Identify the blood parasite species.
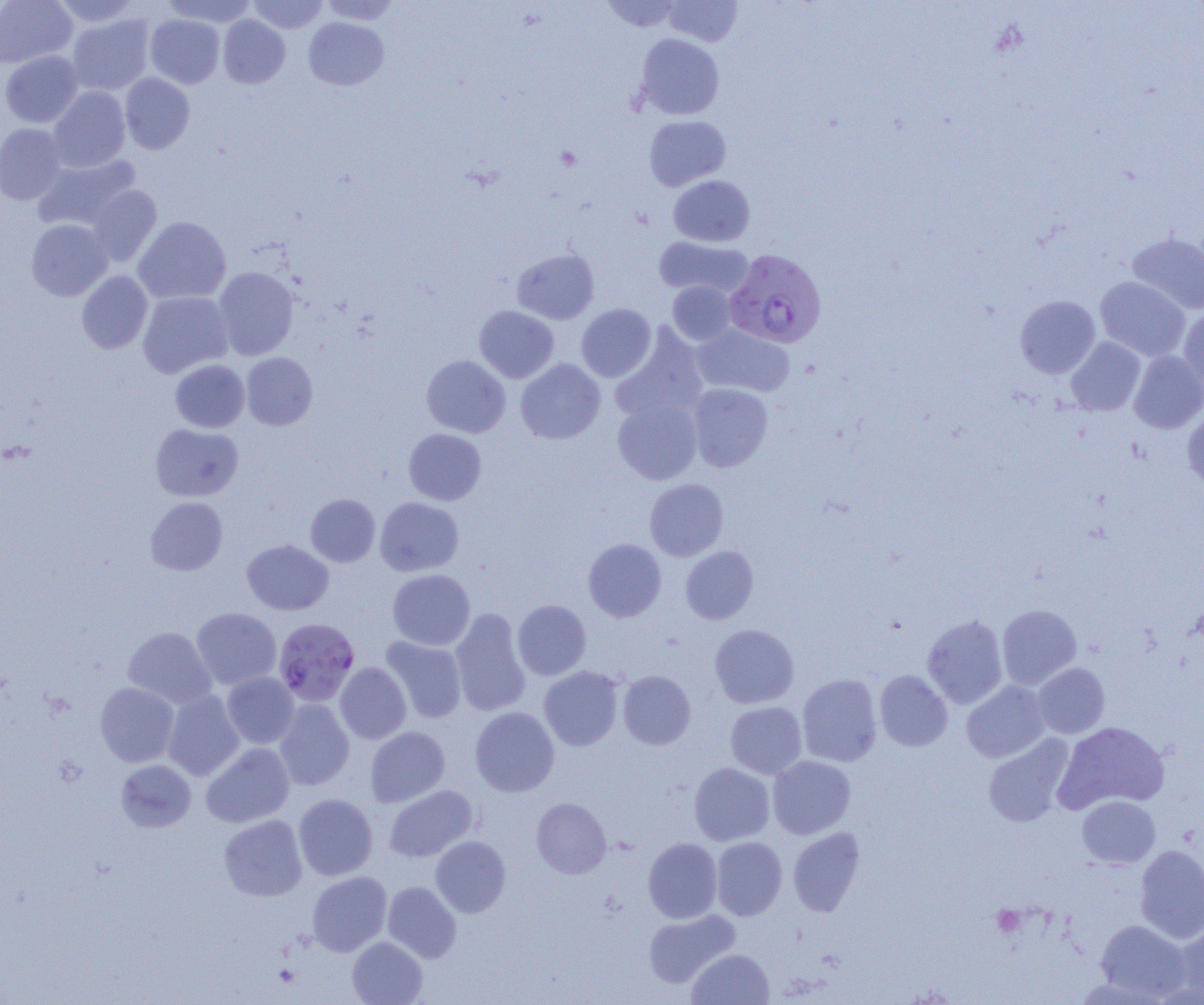

Plasmodium falciparum.

Summary:
  - Coordinate format: approximate bounding boxes as named x1/y1/x2/y2 corners in pixels
  - Plasmodium falciparum-infected red blood cell locations: (x1=724, y1=249, x2=826, y2=348), (x1=275, y1=618, x2=359, y2=706)
  - Uninfected red blood cell locations: (x1=0, y1=0, x2=77, y2=68), (x1=52, y1=0, x2=141, y2=28), (x1=162, y1=0, x2=257, y2=27), (x1=247, y1=0, x2=328, y2=33), (x1=318, y1=0, x2=402, y2=25), (x1=600, y1=0, x2=684, y2=32), (x1=663, y1=0, x2=742, y2=46), (x1=67, y1=14, x2=154, y2=95), (x1=145, y1=14, x2=224, y2=88), (x1=218, y1=14, x2=290, y2=88), (x1=304, y1=17, x2=389, y2=90), (x1=635, y1=33, x2=724, y2=120), (x1=0, y1=51, x2=83, y2=128), (x1=120, y1=73, x2=195, y2=154), (x1=48, y1=87, x2=131, y2=172), (x1=644, y1=115, x2=731, y2=190), (x1=0, y1=124, x2=67, y2=205), (x1=34, y1=154, x2=140, y2=232), (x1=668, y1=175, x2=754, y2=247), (x1=88, y1=185, x2=162, y2=266), (x1=133, y1=216, x2=231, y2=304), (x1=26, y1=219, x2=113, y2=301), (x1=1128, y1=233, x2=1204, y2=315), (x1=655, y1=236, x2=752, y2=299), (x1=512, y1=248, x2=599, y2=324), (x1=213, y1=267, x2=298, y2=360), (x1=77, y1=271, x2=153, y2=354), (x1=1095, y1=276, x2=1190, y2=361), (x1=667, y1=281, x2=736, y2=345), (x1=138, y1=291, x2=233, y2=378), (x1=1015, y1=295, x2=1100, y2=379), (x1=576, y1=304, x2=656, y2=382), (x1=474, y1=306, x2=558, y2=383), (x1=1179, y1=308, x2=1204, y2=390), (x1=691, y1=324, x2=794, y2=397), (x1=611, y1=326, x2=708, y2=424), (x1=1066, y1=337, x2=1145, y2=416), (x1=1128, y1=351, x2=1204, y2=433), (x1=242, y1=352, x2=317, y2=430), (x1=421, y1=355, x2=510, y2=438), (x1=170, y1=359, x2=250, y2=433), (x1=515, y1=359, x2=605, y2=444), (x1=687, y1=383, x2=773, y2=472), (x1=613, y1=398, x2=702, y2=485), (x1=1182, y1=408, x2=1204, y2=490), (x1=150, y1=423, x2=243, y2=501), (x1=404, y1=428, x2=486, y2=505), (x1=645, y1=478, x2=728, y2=561), (x1=305, y1=494, x2=380, y2=567), (x1=144, y1=497, x2=227, y2=575), (x1=375, y1=497, x2=463, y2=576), (x1=583, y1=538, x2=666, y2=622), (x1=242, y1=539, x2=334, y2=615), (x1=680, y1=546, x2=758, y2=624), (x1=387, y1=569, x2=475, y2=650), (x1=512, y1=600, x2=591, y2=680), (x1=997, y1=604, x2=1081, y2=690), (x1=191, y1=608, x2=281, y2=689), (x1=450, y1=608, x2=530, y2=717), (x1=922, y1=615, x2=1008, y2=709), (x1=709, y1=624, x2=799, y2=708), (x1=123, y1=627, x2=216, y2=709), (x1=380, y1=636, x2=467, y2=723), (x1=335, y1=662, x2=411, y2=744), (x1=1032, y1=663, x2=1110, y2=738), (x1=539, y1=666, x2=623, y2=751), (x1=618, y1=670, x2=696, y2=749), (x1=874, y1=670, x2=952, y2=751), (x1=222, y1=673, x2=299, y2=748), (x1=797, y1=674, x2=882, y2=767), (x1=961, y1=680, x2=1051, y2=763), (x1=95, y1=682, x2=179, y2=767), (x1=163, y1=691, x2=244, y2=781), (x1=274, y1=699, x2=354, y2=790), (x1=726, y1=701, x2=807, y2=779), (x1=470, y1=706, x2=560, y2=797), (x1=1054, y1=721, x2=1170, y2=813), (x1=365, y1=727, x2=450, y2=807), (x1=983, y1=735, x2=1075, y2=827), (x1=202, y1=742, x2=294, y2=828), (x1=767, y1=755, x2=855, y2=839), (x1=115, y1=759, x2=196, y2=833), (x1=689, y1=762, x2=775, y2=845), (x1=384, y1=785, x2=477, y2=862), (x1=293, y1=794, x2=378, y2=880), (x1=1077, y1=795, x2=1160, y2=868), (x1=531, y1=798, x2=611, y2=878), (x1=219, y1=814, x2=308, y2=901), (x1=788, y1=828, x2=864, y2=917), (x1=430, y1=836, x2=510, y2=917), (x1=643, y1=837, x2=722, y2=923), (x1=711, y1=837, x2=787, y2=920), (x1=1135, y1=844, x2=1204, y2=943), (x1=307, y1=871, x2=391, y2=956), (x1=382, y1=881, x2=461, y2=963), (x1=643, y1=909, x2=739, y2=987), (x1=1095, y1=920, x2=1190, y2=1001), (x1=1173, y1=923, x2=1204, y2=1003), (x1=347, y1=936, x2=427, y2=1005), (x1=687, y1=949, x2=773, y2=1005)
  - Platelet locations: (x1=992, y1=906, x2=1025, y2=937), (x1=273, y1=964, x2=300, y2=987)
  - Image size: 1204×1005 pixels
  - Magnification: 1000x
  - Field of view: one of a larger specimen
  - Modality: light microscopy
  - Preparation: thin blood smear